Comment on the morphology of the red blood cells.
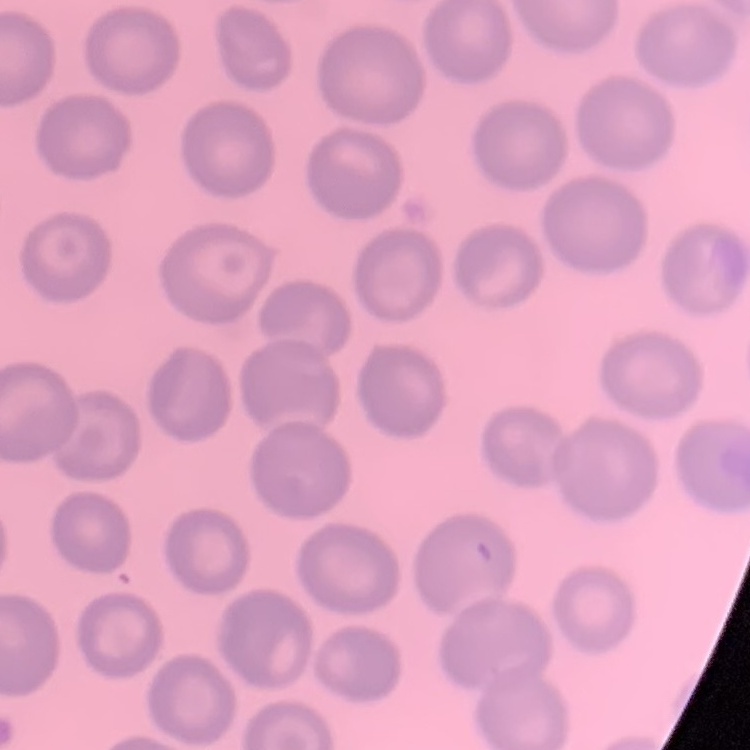

They show no rouleaux formation.

Summary:
  - Image type: square crop of a larger photomicrograph
  - Preparation: thin blood film
  - Stain: Field's or Giemsa